Assess for malaria.
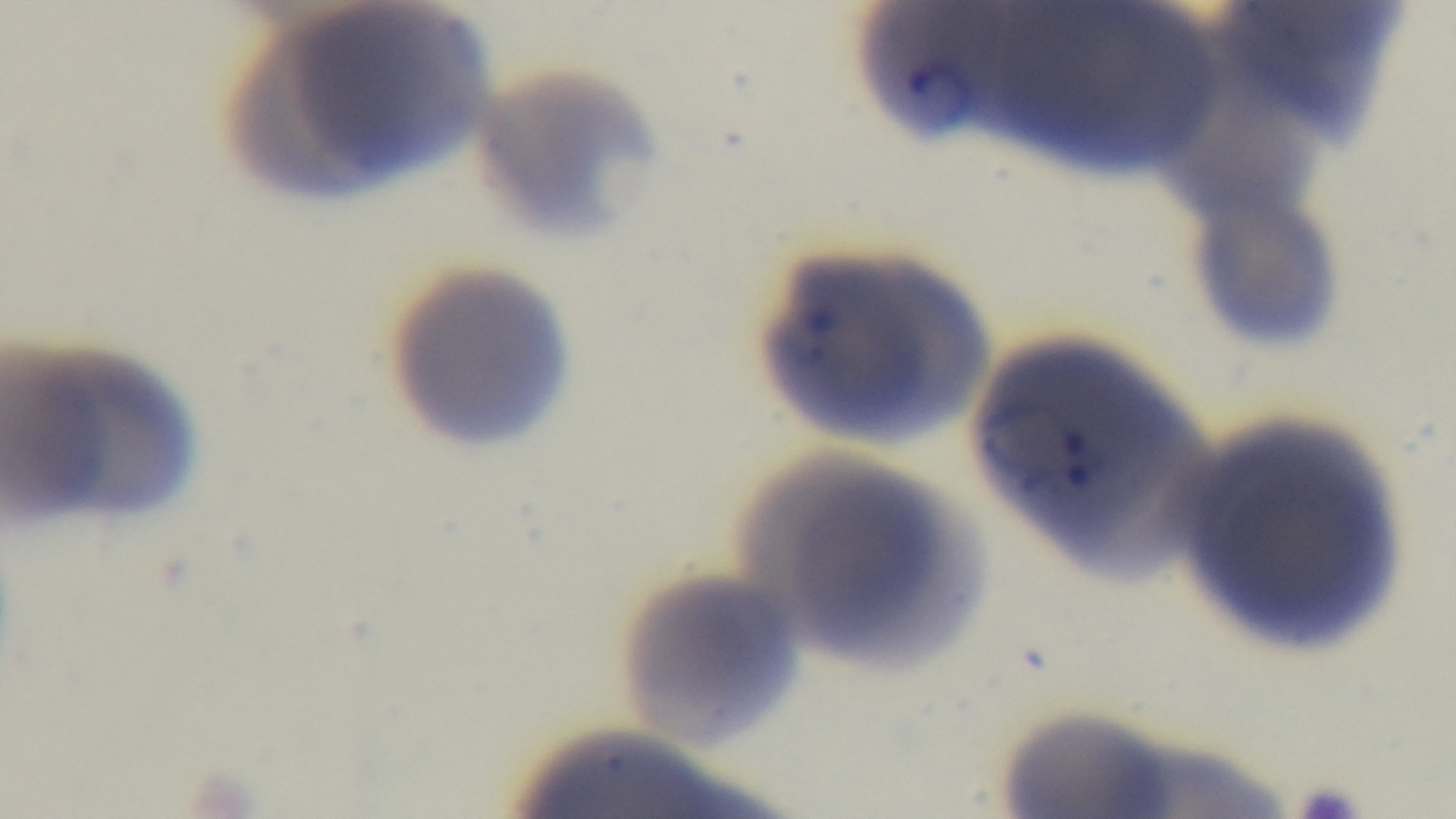
Positive.

{
  "modality": "light microscopy",
  "capture": "mounted 4K digital camera",
  "objective": "100x oil immersion",
  "stain": "Giemsa",
  "field_of_view": "single",
  "preparation": "thin smear"
}